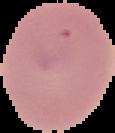

image size = 115×133 pixels
image type = cell region segmented out of the field of view; surrounding area masked to black
preparation = thin blood film
malaria status = uninfected